State the blood parasite species.
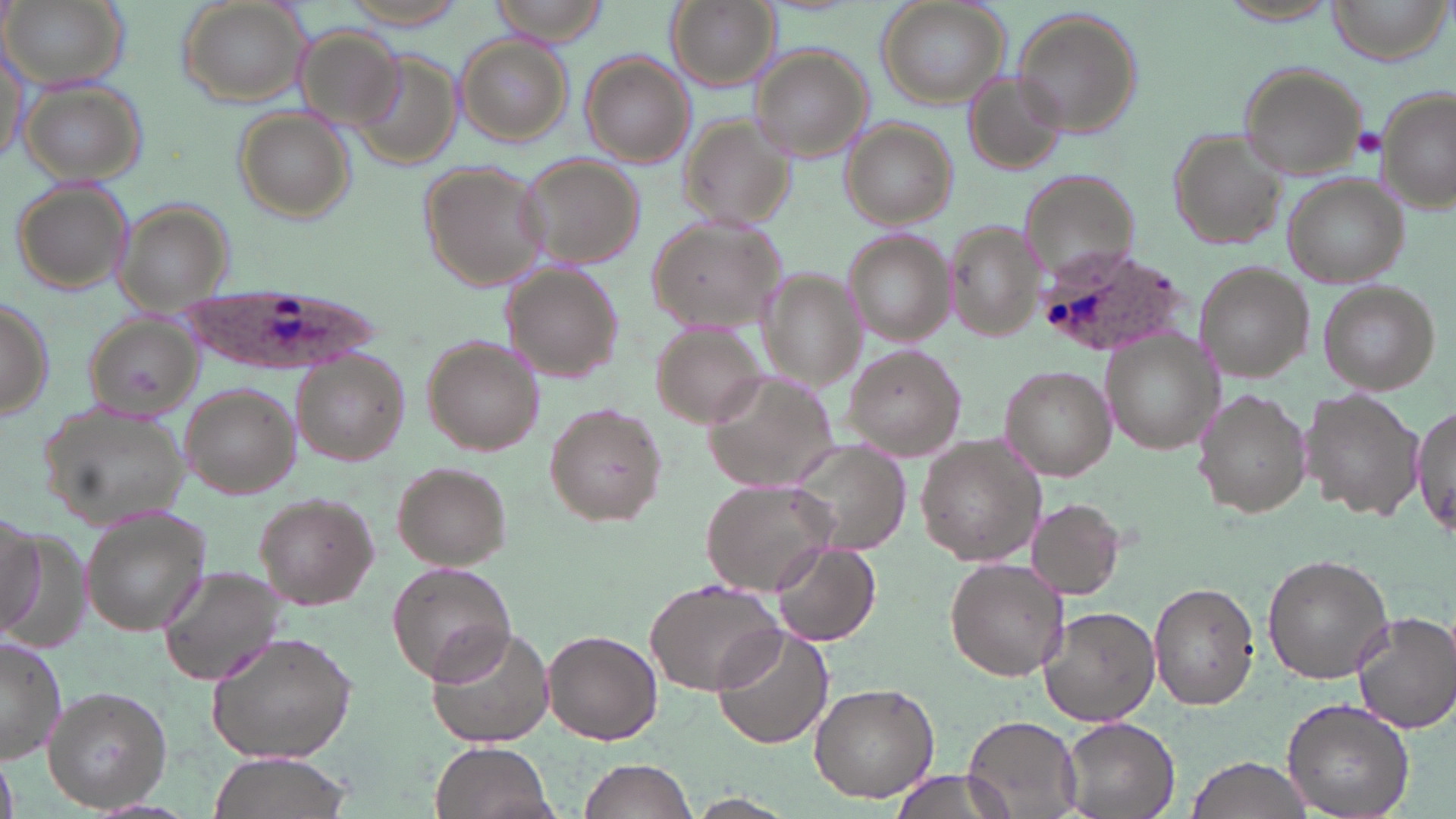
Plasmodium ovale.

Summary:
  - Coordinate format: approximate bounding boxes as [x1, y1, x2, y2] in pixels
  - Uninfected red blood cell locations: [1, 0, 129, 92], [491, 0, 613, 42], [666, 0, 778, 90], [874, 0, 1010, 108], [1328, 0, 1450, 66], [175, 1, 310, 110], [1213, 1, 1341, 25], [1010, 7, 1144, 142], [456, 35, 573, 148], [1, 44, 29, 169], [350, 45, 461, 167], [748, 47, 873, 165], [580, 54, 695, 168], [1237, 62, 1367, 177], [965, 72, 1066, 172], [20, 79, 147, 186], [1375, 87, 1455, 215], [235, 107, 356, 223], [680, 115, 797, 231], [841, 117, 959, 229], [1167, 128, 1286, 249], [517, 154, 646, 272], [416, 160, 550, 292], [1022, 171, 1135, 286], [1285, 178, 1407, 288], [10, 182, 136, 294], [111, 199, 233, 303], [646, 217, 787, 330], [949, 223, 1042, 340], [840, 231, 952, 345], [1194, 264, 1313, 384], [505, 266, 626, 384], [756, 268, 865, 388], [1318, 280, 1440, 393], [0, 294, 54, 422], [81, 313, 200, 419], [649, 319, 770, 430], [1102, 334, 1220, 456], [421, 336, 545, 457], [841, 344, 964, 459], [291, 352, 409, 464], [1001, 364, 1117, 478], [704, 368, 842, 494], [179, 384, 302, 497], [1299, 387, 1426, 520], [1194, 390, 1312, 518], [545, 401, 668, 528], [38, 403, 195, 531], [1410, 403, 1455, 544], [915, 434, 1046, 567], [784, 440, 911, 558], [392, 463, 512, 570], [701, 480, 838, 595], [254, 493, 380, 607], [1026, 498, 1125, 599], [78, 509, 212, 634], [0, 515, 53, 639], [773, 540, 880, 646], [1263, 553, 1392, 685], [945, 556, 1068, 681], [386, 561, 516, 684], [155, 566, 286, 689], [645, 576, 786, 695], [1151, 582, 1261, 711], [1039, 604, 1162, 728], [1351, 611, 1456, 733], [423, 622, 557, 751], [710, 626, 835, 751], [543, 629, 663, 745], [206, 632, 358, 764], [0, 634, 67, 763], [809, 682, 940, 803], [41, 686, 173, 812], [1282, 698, 1415, 819], [964, 715, 1083, 818], [1061, 716, 1181, 819], [430, 741, 556, 819], [0, 751, 16, 819], [205, 752, 358, 819], [1187, 754, 1314, 819], [580, 758, 698, 818], [889, 768, 1021, 817], [684, 794, 797, 819]
  - Plasmodium ovale-infected red blood cell locations: [1040, 250, 1190, 359], [181, 284, 375, 372]
  - Platelet locations: [1355, 127, 1385, 156]
  - Image size: 1456×819 pixels
  - Modality: light microscopy
  - Stain: May-Grünwald-Giemsa
  - Preparation: thin blood smear
  - Magnification: 1000x
  - Field of view: single